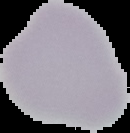

image size = 130×133 pixels
malaria status = uninfected
image type = cell region segmented out of the field of view; surrounding area masked to black
preparation = thin blood film